Locate the P. falciparum-infected red blood cells and any of indeterminate infection status.
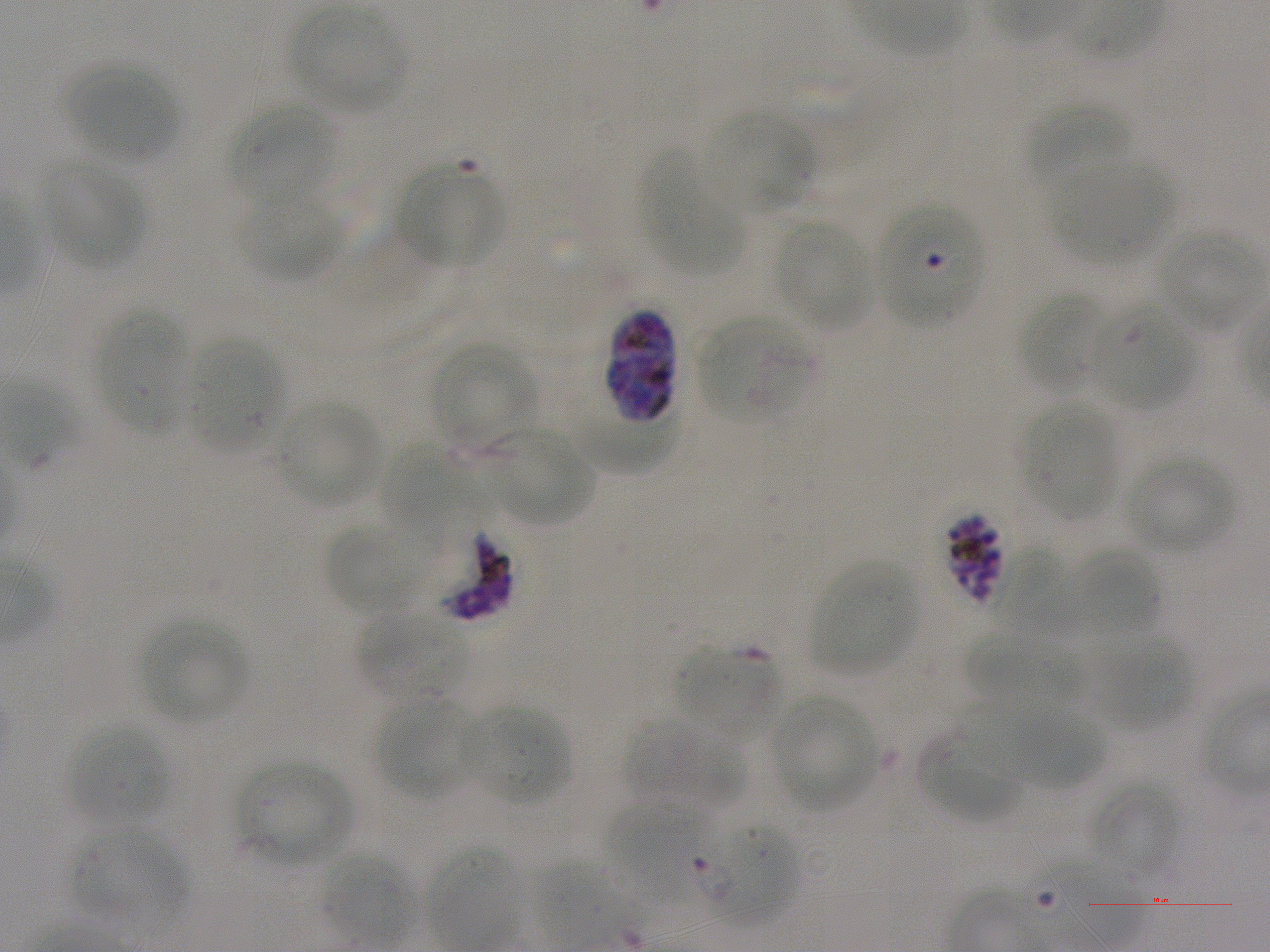

Approximate bounding rectangles given as corner coordinates in pixels from the top-left. Not every red blood cell is marked. A life-cycle stage — or a range of stages, where the recorded stages span more than one — follows each staged infected red blood cell.
Infected red blood cells: (x1=878, y1=206, x2=982, y2=326); (x1=603, y1=307, x2=679, y2=423); (x1=943, y1=512, x2=1007, y2=607) schizont.
Red blood cells of indeterminate infection status: (x1=698, y1=318, x2=810, y2=424), (x1=432, y1=526, x2=520, y2=622), (x1=991, y1=548, x2=1076, y2=634), (x1=463, y1=705, x2=570, y2=806), (x1=701, y1=821, x2=799, y2=924).

{
  "locations_of_uninfected_red_blood_cells": "(x1=292, y1=8, x2=407, y2=113), (x1=69, y1=65, x2=176, y2=163), (x1=1024, y1=100, x2=1134, y2=193), (x1=231, y1=101, x2=334, y2=208), (x1=703, y1=111, x2=811, y2=217), (x1=641, y1=148, x2=743, y2=276), (x1=43, y1=159, x2=144, y2=268), (x1=1052, y1=162, x2=1172, y2=263), (x1=398, y1=163, x2=503, y2=270), (x1=238, y1=190, x2=343, y2=282), (x1=775, y1=221, x2=872, y2=330), (x1=1155, y1=230, x2=1260, y2=334), (x1=1020, y1=291, x2=1108, y2=393), (x1=1089, y1=300, x2=1195, y2=412), (x1=97, y1=311, x2=190, y2=436), (x1=189, y1=339, x2=285, y2=456), (x1=431, y1=342, x2=538, y2=447), (x1=277, y1=401, x2=380, y2=506), (x1=1023, y1=403, x2=1117, y2=520), (x1=565, y1=415, x2=676, y2=471), (x1=486, y1=424, x2=595, y2=526), (x1=380, y1=441, x2=494, y2=553), (x1=1123, y1=455, x2=1237, y2=555), (x1=324, y1=522, x2=427, y2=615), (x1=1069, y1=548, x2=1160, y2=637), (x1=811, y1=560, x2=918, y2=675), (x1=360, y1=613, x2=468, y2=704), (x1=141, y1=619, x2=250, y2=725), (x1=964, y1=630, x2=1084, y2=709), (x1=1090, y1=635, x2=1193, y2=731), (x1=676, y1=645, x2=781, y2=743), (x1=771, y1=695, x2=878, y2=812), (x1=373, y1=698, x2=476, y2=800), (x1=960, y1=699, x2=1060, y2=778), (x1=1006, y1=704, x2=1104, y2=788), (x1=623, y1=720, x2=745, y2=811), (x1=66, y1=725, x2=171, y2=828), (x1=918, y1=734, x2=1022, y2=823), (x1=237, y1=760, x2=351, y2=866), (x1=1088, y1=780, x2=1181, y2=882), (x1=606, y1=800, x2=709, y2=900), (x1=66, y1=829, x2=189, y2=926), (x1=426, y1=845, x2=520, y2=949), (x1=324, y1=852, x2=413, y2=946)",
  "preparation": "thin blood smear",
  "field_of_view": "one from this slide",
  "objective": "100x, oil immersion, numerical aperture 1.25",
  "stain": "Giemsa",
  "culture": "static in-vitro P. falciparum strain NF54",
  "donor_blood_group": "A+",
  "image_size": "1270×952 pixels"
}